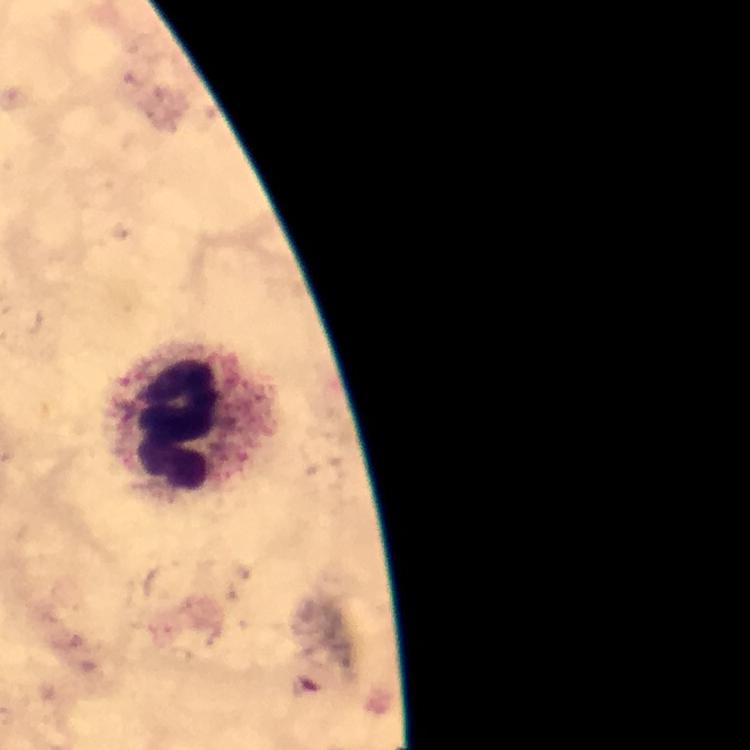

Approximate centers as [x, y] in pixels.
Summary:
  - Leukocyte locations: [184, 419]
  - Image size: 750×750 pixels
  - Immersion oil: used
  - Capture: smartphone camera through the microscope
  - Cropped from: a single field of view
  - Plasmodium parasites: none detected
  - Preparation: thick smear
  - Context: from a diagnostic examination for malaria
  - Magnification: 100x
  - Stain: Giemsa